Report the malaria status of this cell.
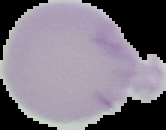
It is uninfected.

Summary:
  - Image type: segmented cell region with the area outside set to black
  - Image size: 166×130 pixels
  - Preparation: thin blood film